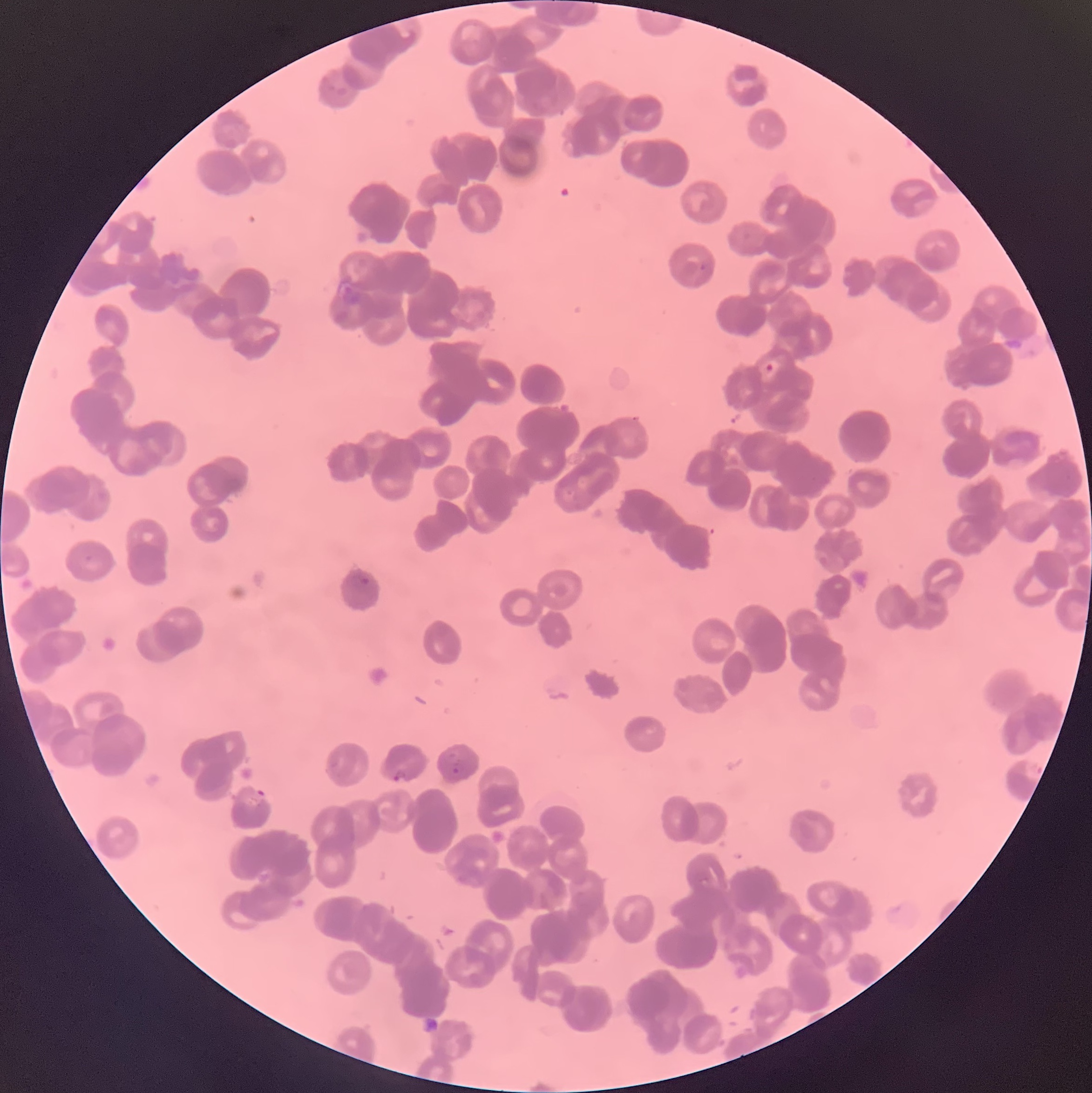

coordinate format = approximate bounding boxes as named x1/y1/x2/y2 corners in pixels
Plasmodium parasite locations = (x1=765, y1=363, x2=773, y2=373), (x1=361, y1=576, x2=370, y2=587), (x1=452, y1=767, x2=461, y2=775), (x1=393, y1=770, x2=406, y2=783), (x1=253, y1=788, x2=265, y2=801)
modality = optical microscopy
image size = 1092×1093 pixels
preparation = thin blood smear
red blood cell morphology = rouleaux formation